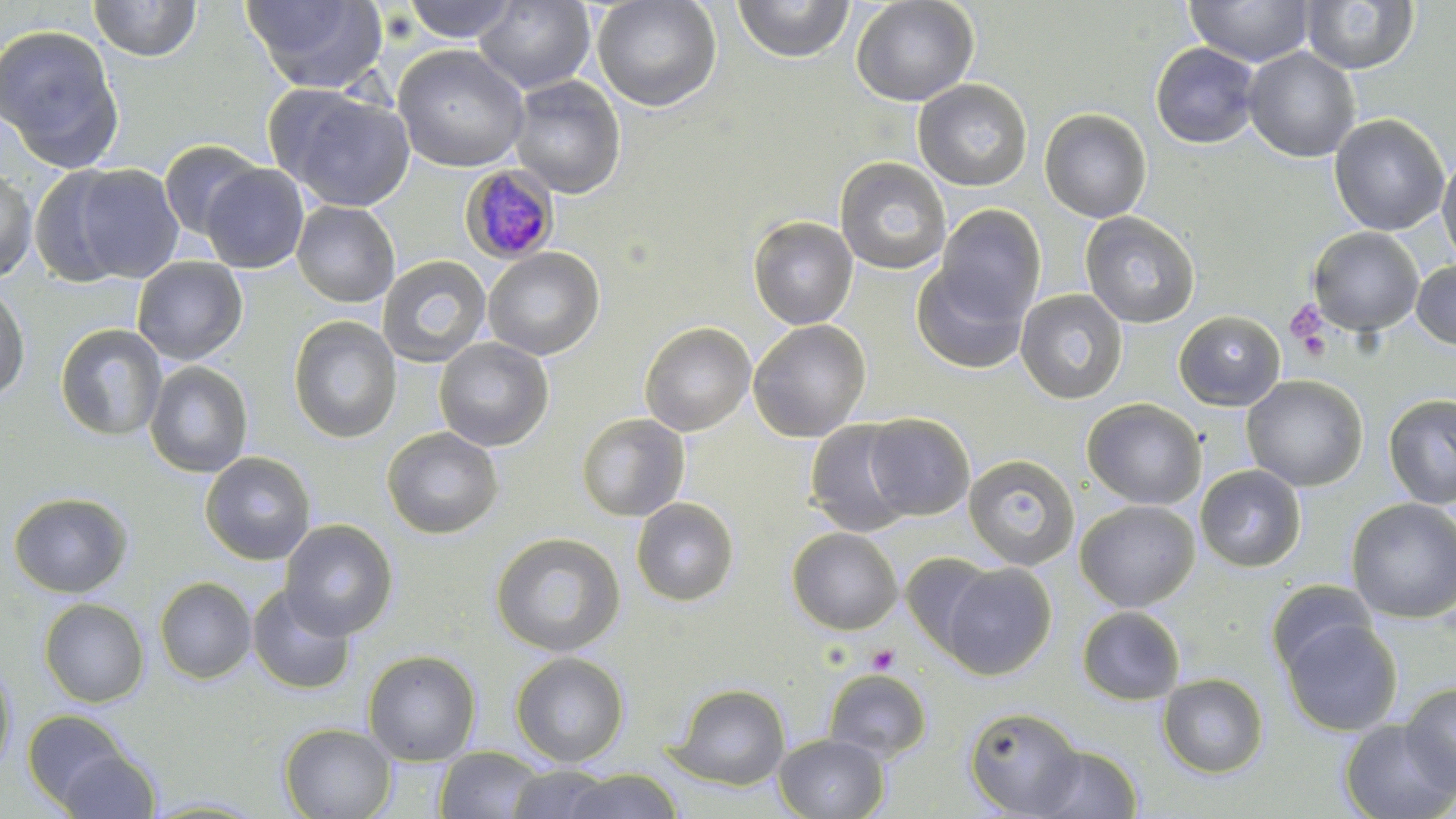
Summary:
  - Coordinate format: approximate bounding boxes as named x1/y1/x2/y2 corners in pixels
  - Plasmodium malariae-infected red blood cell locations: (x1=460, y1=166, x2=559, y2=264)
  - Platelet locations: (x1=1285, y1=301, x2=1329, y2=348), (x1=1296, y1=329, x2=1331, y2=362), (x1=865, y1=644, x2=900, y2=675)
  - Uninfected red blood cell locations: (x1=88, y1=0, x2=202, y2=62), (x1=242, y1=0, x2=388, y2=94), (x1=401, y1=0, x2=519, y2=43), (x1=473, y1=0, x2=596, y2=93), (x1=592, y1=0, x2=722, y2=112), (x1=732, y1=0, x2=855, y2=63), (x1=850, y1=0, x2=979, y2=106), (x1=1184, y1=0, x2=1316, y2=67), (x1=1300, y1=0, x2=1419, y2=74), (x1=0, y1=24, x2=125, y2=172), (x1=1150, y1=42, x2=1261, y2=149), (x1=392, y1=44, x2=529, y2=172), (x1=1243, y1=46, x2=1361, y2=162), (x1=508, y1=75, x2=626, y2=199), (x1=913, y1=79, x2=1033, y2=191), (x1=273, y1=87, x2=416, y2=212), (x1=1040, y1=108, x2=1152, y2=223), (x1=1329, y1=113, x2=1450, y2=237), (x1=158, y1=139, x2=266, y2=241), (x1=1437, y1=151, x2=1456, y2=270), (x1=834, y1=157, x2=952, y2=275), (x1=67, y1=164, x2=184, y2=284), (x1=200, y1=164, x2=309, y2=273), (x1=0, y1=166, x2=37, y2=283), (x1=27, y1=167, x2=135, y2=287), (x1=291, y1=201, x2=400, y2=307), (x1=934, y1=205, x2=1046, y2=324), (x1=1080, y1=211, x2=1200, y2=328), (x1=748, y1=215, x2=858, y2=329), (x1=1307, y1=227, x2=1424, y2=335), (x1=483, y1=247, x2=605, y2=360), (x1=377, y1=255, x2=491, y2=367), (x1=131, y1=257, x2=248, y2=365), (x1=1411, y1=260, x2=1456, y2=351), (x1=911, y1=263, x2=1030, y2=374), (x1=0, y1=281, x2=31, y2=402), (x1=1015, y1=288, x2=1128, y2=404), (x1=1174, y1=310, x2=1286, y2=411), (x1=288, y1=315, x2=401, y2=444), (x1=748, y1=319, x2=871, y2=442), (x1=639, y1=321, x2=756, y2=435), (x1=55, y1=324, x2=167, y2=441), (x1=433, y1=336, x2=554, y2=451), (x1=144, y1=361, x2=254, y2=478), (x1=1241, y1=374, x2=1369, y2=491), (x1=1383, y1=393, x2=1456, y2=509), (x1=1082, y1=398, x2=1206, y2=509), (x1=575, y1=413, x2=690, y2=522), (x1=863, y1=413, x2=975, y2=520), (x1=804, y1=419, x2=918, y2=537), (x1=381, y1=426, x2=503, y2=539), (x1=200, y1=452, x2=317, y2=565), (x1=963, y1=454, x2=1079, y2=571), (x1=1195, y1=464, x2=1307, y2=572), (x1=8, y1=491, x2=134, y2=598), (x1=631, y1=497, x2=739, y2=606), (x1=1345, y1=497, x2=1456, y2=623), (x1=1074, y1=499, x2=1200, y2=611), (x1=280, y1=519, x2=398, y2=639), (x1=786, y1=528, x2=902, y2=635), (x1=490, y1=532, x2=626, y2=657), (x1=902, y1=552, x2=1000, y2=656), (x1=940, y1=562, x2=1056, y2=679), (x1=155, y1=577, x2=257, y2=684), (x1=1265, y1=579, x2=1378, y2=678), (x1=247, y1=584, x2=355, y2=694), (x1=39, y1=598, x2=149, y2=707), (x1=1076, y1=606, x2=1185, y2=705), (x1=1282, y1=618, x2=1402, y2=735), (x1=362, y1=649, x2=481, y2=765), (x1=511, y1=652, x2=629, y2=767), (x1=0, y1=658, x2=16, y2=777), (x1=823, y1=669, x2=932, y2=763), (x1=1157, y1=673, x2=1269, y2=778), (x1=1400, y1=681, x2=1456, y2=794), (x1=670, y1=683, x2=791, y2=790), (x1=964, y1=706, x2=1085, y2=817), (x1=23, y1=710, x2=133, y2=810), (x1=1338, y1=719, x2=1455, y2=819), (x1=279, y1=723, x2=397, y2=818), (x1=774, y1=733, x2=888, y2=818), (x1=1031, y1=745, x2=1143, y2=818), (x1=54, y1=747, x2=162, y2=819), (x1=434, y1=747, x2=547, y2=819), (x1=505, y1=764, x2=617, y2=818), (x1=562, y1=769, x2=685, y2=819)
  - Slide-level diagnosis: Plasmodium malariae
  - Field of view: one of a larger specimen
  - Stain: May-Grünwald-Giemsa
  - Magnification: 1000x
  - Preparation: thin blood smear
  - Modality: optical microscopy
  - Image size: 1456×819 pixels